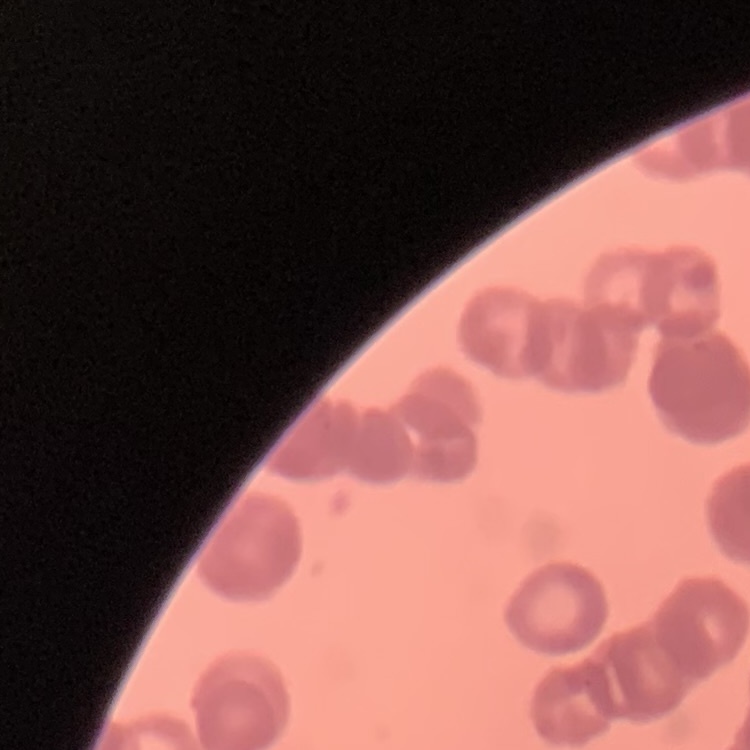
erythrocyte morphology = rouleaux formation
stain = Field's or Giemsa
preparation = thin blood smear
image type = square crop of a larger photomicrograph